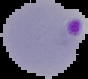
Summary:
  - Preparation: thin blood film
  - Image type: segmented cell region on a black background
  - Image size: 88×79 pixels
  - Malaria status: parasitized